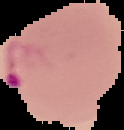 Segmented cell region on a black background. Malaria status: parasitized. From a thin blood film. Image is 124×130 pixels.